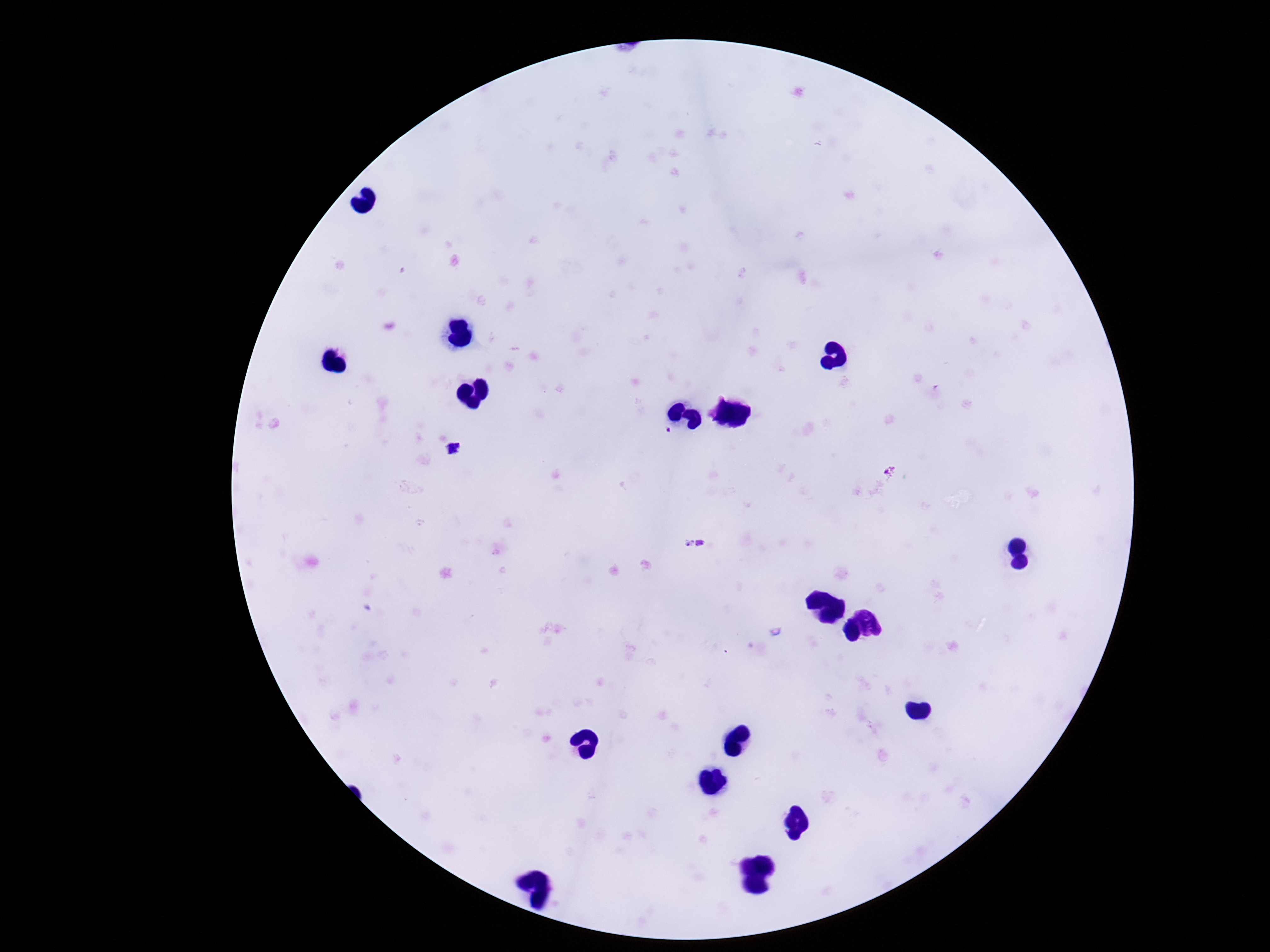 Approximate object centers, in pixels from the top-left corner. Plasmodium parasite locations: (x=666, y=432), (x=696, y=544). One field from this slide. Thick blood film. Smartphone photograph taken through the microscope eyepiece. Image is 1270×952 pixels. 100x magnification. Giemsa-stained preparation. Patient malaria status: infected.